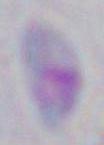
1000x magnification. Photomicrograph. Toxoplasma gondii is seen.